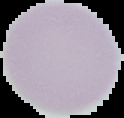
Summary:
  - Malaria status: uninfected
  - Preparation: thin blood film
  - Image type: cell region segmented out of the field of view; surrounding area masked to black
  - Image size: 124×118 pixels